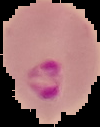
Image is 100×127 pixels. From a thin blood film. Result: Plasmodium parasites identified. Cell region segmented out of the field of view; the surrounding area is masked to black.